Outline platelets.
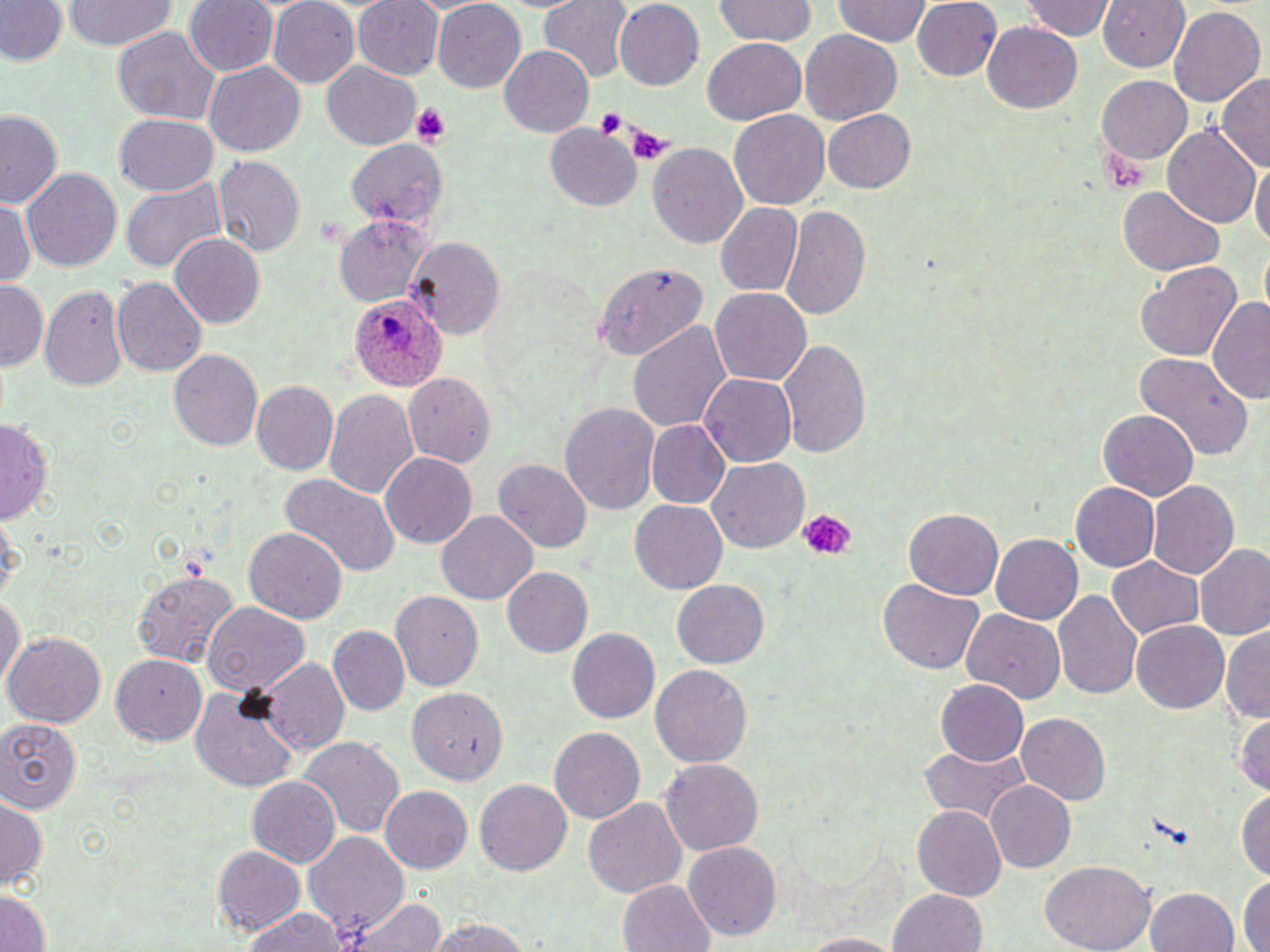
Approximate bounding boxes as [x1, y1, x2, y2] in pixels.
Platelets: [410, 103, 452, 145], [595, 107, 626, 138], [625, 123, 672, 165], [797, 510, 857, 560].

Uninfected red blood cell locations: [65, 0, 175, 50], [186, 0, 279, 77], [538, 0, 635, 81], [612, 0, 704, 91], [713, 0, 818, 45], [832, 0, 929, 44], [912, 0, 1001, 80], [1099, 0, 1190, 72], [0, 1, 68, 65], [267, 1, 360, 87], [353, 1, 445, 79], [1017, 1, 1116, 42], [432, 2, 527, 92], [1169, 6, 1264, 106], [982, 21, 1081, 114], [111, 26, 220, 125], [800, 27, 903, 125], [701, 37, 808, 126], [498, 44, 594, 136], [204, 60, 306, 156], [322, 61, 420, 149], [1217, 73, 1270, 171], [1097, 75, 1190, 164], [821, 109, 916, 192], [729, 110, 830, 210], [0, 111, 64, 208], [113, 112, 219, 196], [545, 123, 640, 212], [1163, 126, 1260, 231], [344, 139, 451, 230], [647, 142, 747, 249], [212, 155, 306, 258], [1250, 159, 1270, 250], [21, 167, 123, 270], [120, 180, 227, 272], [1119, 186, 1224, 277], [1, 198, 35, 285], [714, 201, 801, 295], [779, 204, 870, 320], [333, 215, 433, 306], [169, 233, 263, 326], [407, 237, 506, 339], [1260, 242, 1269, 321], [1134, 261, 1240, 361], [593, 263, 707, 358], [110, 277, 208, 377], [1, 281, 46, 370], [39, 283, 129, 391], [710, 287, 811, 387], [1208, 296, 1270, 405], [628, 321, 731, 432], [778, 337, 871, 459], [167, 348, 262, 451], [1136, 352, 1252, 461], [401, 372, 496, 468], [699, 372, 797, 466], [249, 379, 339, 475], [324, 389, 418, 497], [560, 401, 662, 514], [1099, 411, 1198, 499], [0, 419, 53, 522], [645, 420, 729, 508], [380, 452, 477, 547], [493, 457, 592, 552], [706, 457, 808, 552], [278, 473, 399, 575], [1148, 481, 1239, 579], [1071, 482, 1160, 572], [630, 499, 726, 592], [904, 507, 1003, 600], [436, 510, 540, 605], [0, 511, 24, 603], [242, 527, 347, 625], [992, 533, 1083, 623], [1195, 544, 1269, 639], [1106, 556, 1203, 638], [502, 566, 594, 657], [130, 568, 239, 667], [672, 579, 769, 668], [879, 579, 983, 674], [1053, 589, 1142, 700], [390, 590, 484, 690], [0, 593, 23, 690], [201, 601, 309, 694], [962, 608, 1064, 705], [1132, 620, 1230, 712], [328, 625, 410, 715], [1221, 625, 1270, 724], [566, 627, 660, 722], [5, 630, 107, 727], [111, 652, 208, 744], [261, 657, 351, 756], [650, 664, 753, 768], [935, 679, 1026, 765], [190, 684, 297, 792], [408, 687, 508, 785], [1233, 710, 1269, 796], [1016, 713, 1111, 804], [0, 719, 81, 812], [549, 726, 645, 822], [299, 735, 404, 838], [918, 746, 1026, 822], [659, 756, 764, 856], [245, 775, 340, 867], [475, 778, 571, 875], [985, 780, 1075, 872], [380, 784, 472, 872], [1236, 787, 1269, 880], [0, 792, 47, 890], [583, 797, 686, 898], [912, 803, 1006, 901], [305, 830, 408, 936], [681, 840, 781, 941], [212, 844, 306, 935], [1041, 860, 1155, 952], [1239, 876, 1269, 951], [616, 878, 715, 952], [887, 887, 986, 952], [1147, 888, 1238, 952], [0, 891, 51, 952], [344, 898, 448, 952], [243, 909, 348, 952], [423, 917, 541, 951], [798, 933, 904, 951]. Plasmodium ovale-infected red blood cell locations: [348, 294, 448, 388]. Slide-level diagnosis: Plasmodium ovale. One field of a larger specimen. Image is 1270×952 pixels. Captured at 1000x magnification. May-Grünwald-Giemsa-stained preparation. Thin blood film. Light microscopy.